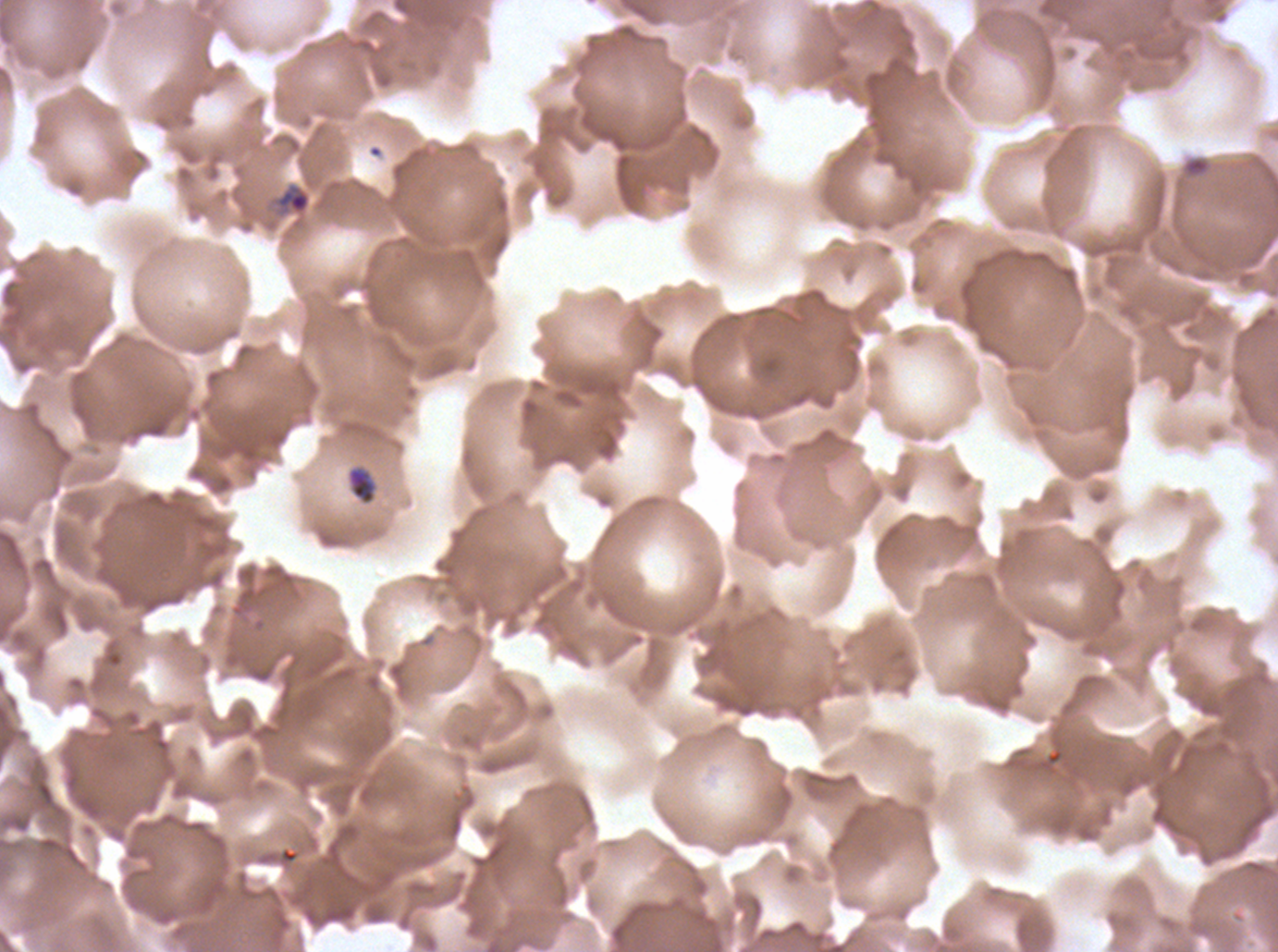

Approximate bounding boxes as {x1, y1, x2, y2} in pixels. Object labeled both ring and debris by the source: {274, 182, 312, 215}. Debris locations: {1181, 155, 1211, 179}. Late-ring/early-trophozoite locations: {347, 466, 377, 506}. Image is 1278×952 pixels. Ex-vivo Plasmodium falciparum culture from a patient in The Gambia, grown for 24 to 48 hours. Thin blood smear. Giemsa-stained preparation. A sub-image separated from a larger composite.